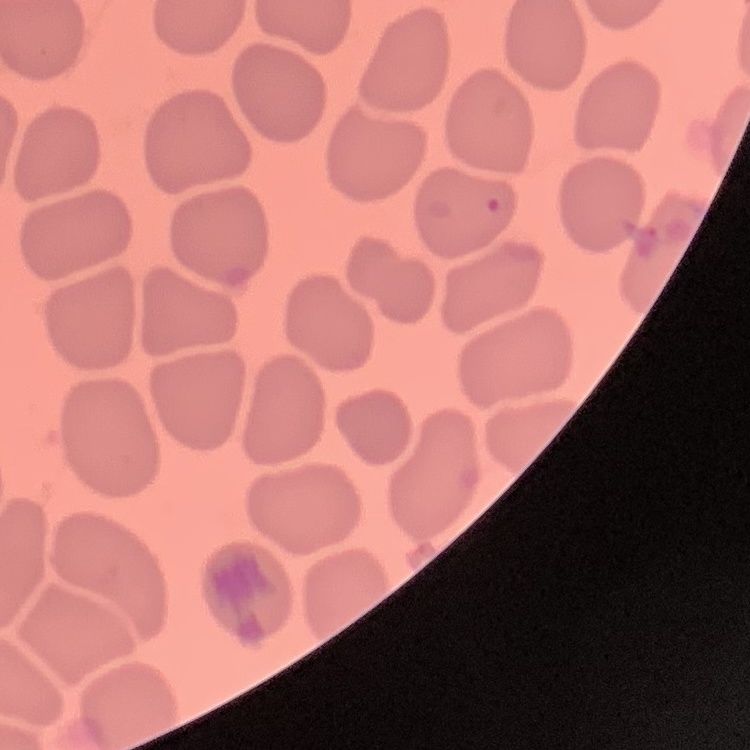 The red blood cells exhibit no rouleaux formation. One tile cut from a larger photomicrograph. Thin peripheral smear. Field's or Giemsa stain.